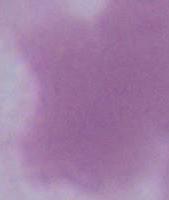
identification = erythrocyte
modality = photomicrograph
magnification = 1000x